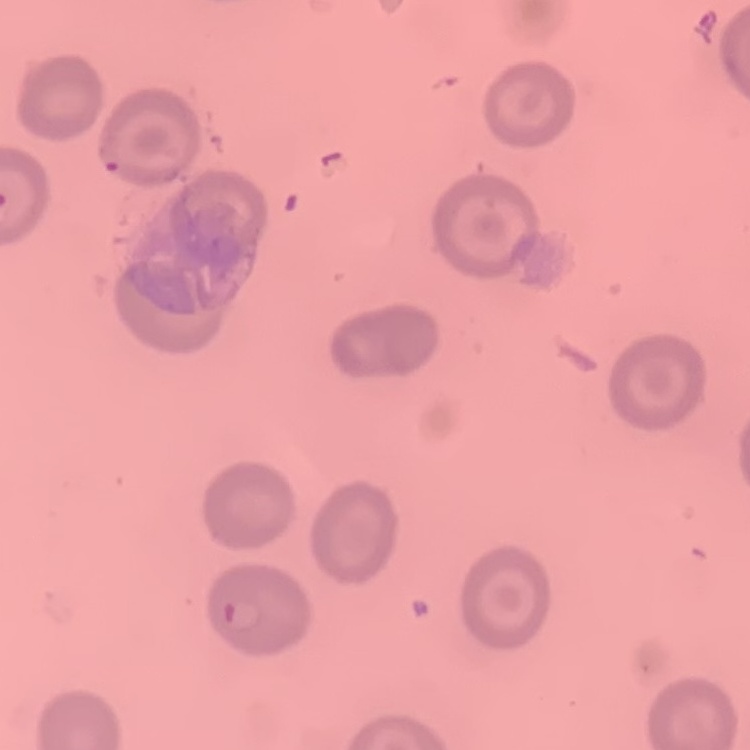

Summary:
  - Erythrocyte morphology: no rouleaux formation
  - Preparation: thin peripheral smear
  - Stain: Field's or Giemsa
  - Image type: square crop of a larger photomicrograph